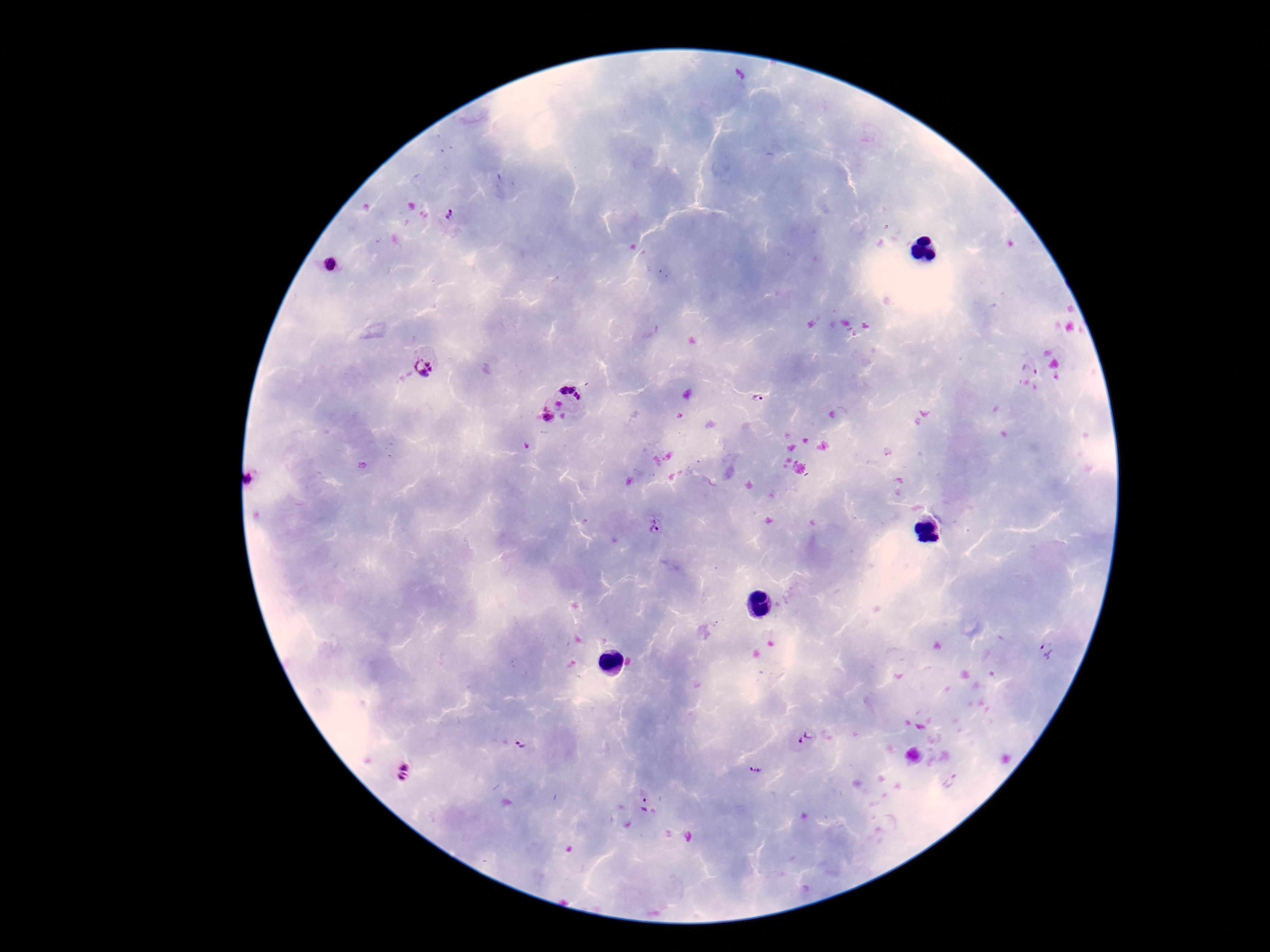
Approximate centers as {x, y} in pixels. Plasmodium parasite locations: {450, 221}, {336, 268}, {424, 367}, {1031, 367}, {572, 391}, {759, 399}, {547, 417}, {254, 477}, {654, 525}, {1048, 652}, {805, 739}, {522, 746}, {757, 771}, {404, 772}, {954, 782}, {643, 803}. 100x magnification. Patient malaria status: infected. Thick peripheral-blood smear. Giemsa-stained preparation. Smartphone photograph taken through the microscope eyepiece. Image is 1270×952 pixels. Single field of view.